Give the position of every leukocyte visible.
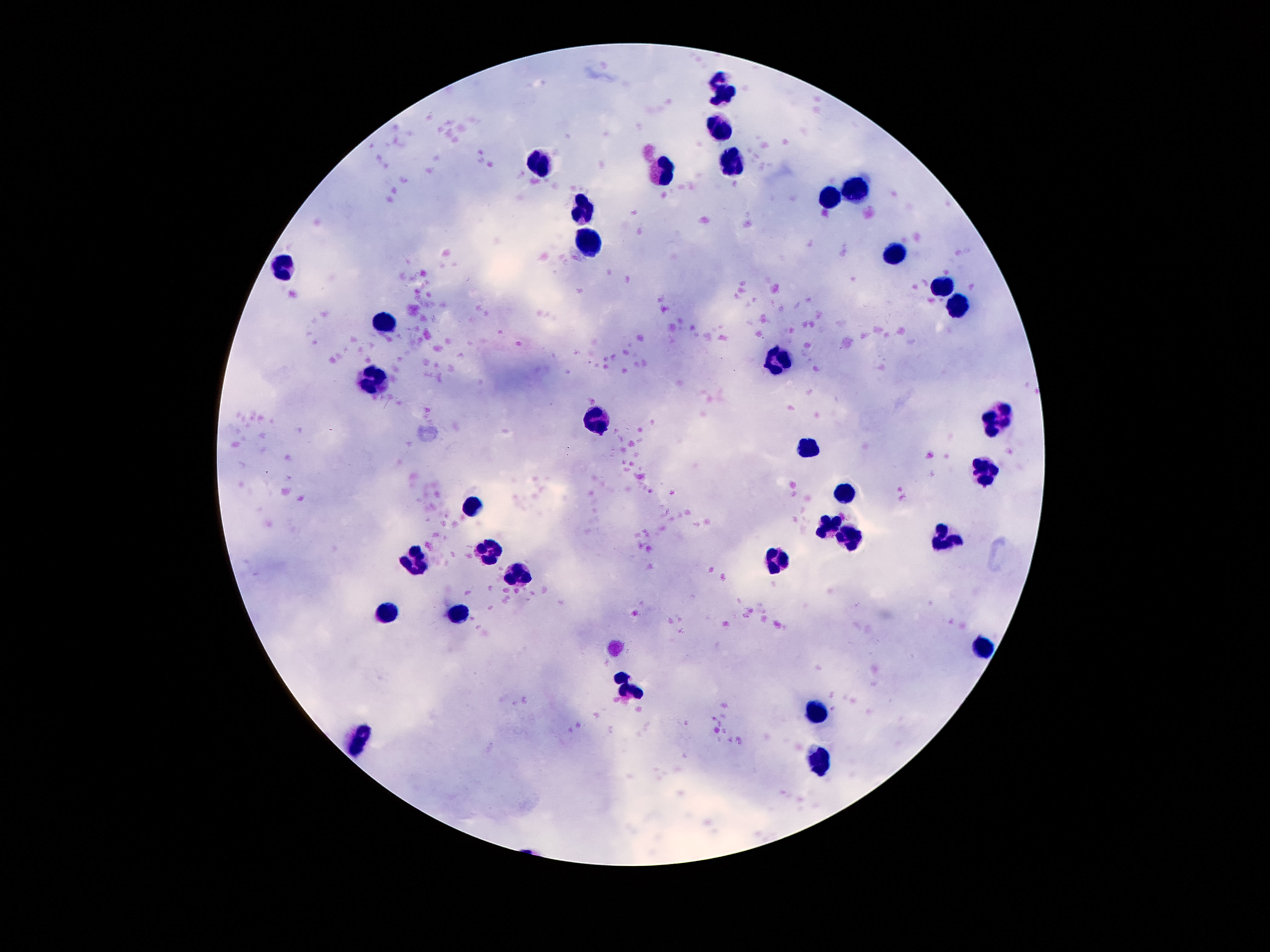
Approximate centers as (x, y) in pixels.
Leukocytes: (721, 89), (717, 129), (733, 157), (542, 164), (665, 173), (855, 190), (826, 198), (582, 208), (589, 243), (894, 255), (281, 261), (941, 287), (955, 306), (386, 320), (777, 358), (376, 381), (995, 418), (594, 422), (808, 446), (983, 472), (843, 497), (472, 507), (831, 525), (852, 539), (946, 540), (491, 551), (416, 560), (773, 560), (519, 574), (458, 612), (388, 614), (980, 647), (626, 689), (815, 710), (360, 736), (822, 762).

{
  "capture": "smartphone camera through the microscope eyepiece",
  "magnification": "100x",
  "stain": "Giemsa",
  "image_size": "1270×952 pixels",
  "patient_malaria_status": "negative",
  "preparation": "thick blood film",
  "field_of_view": "single"
}